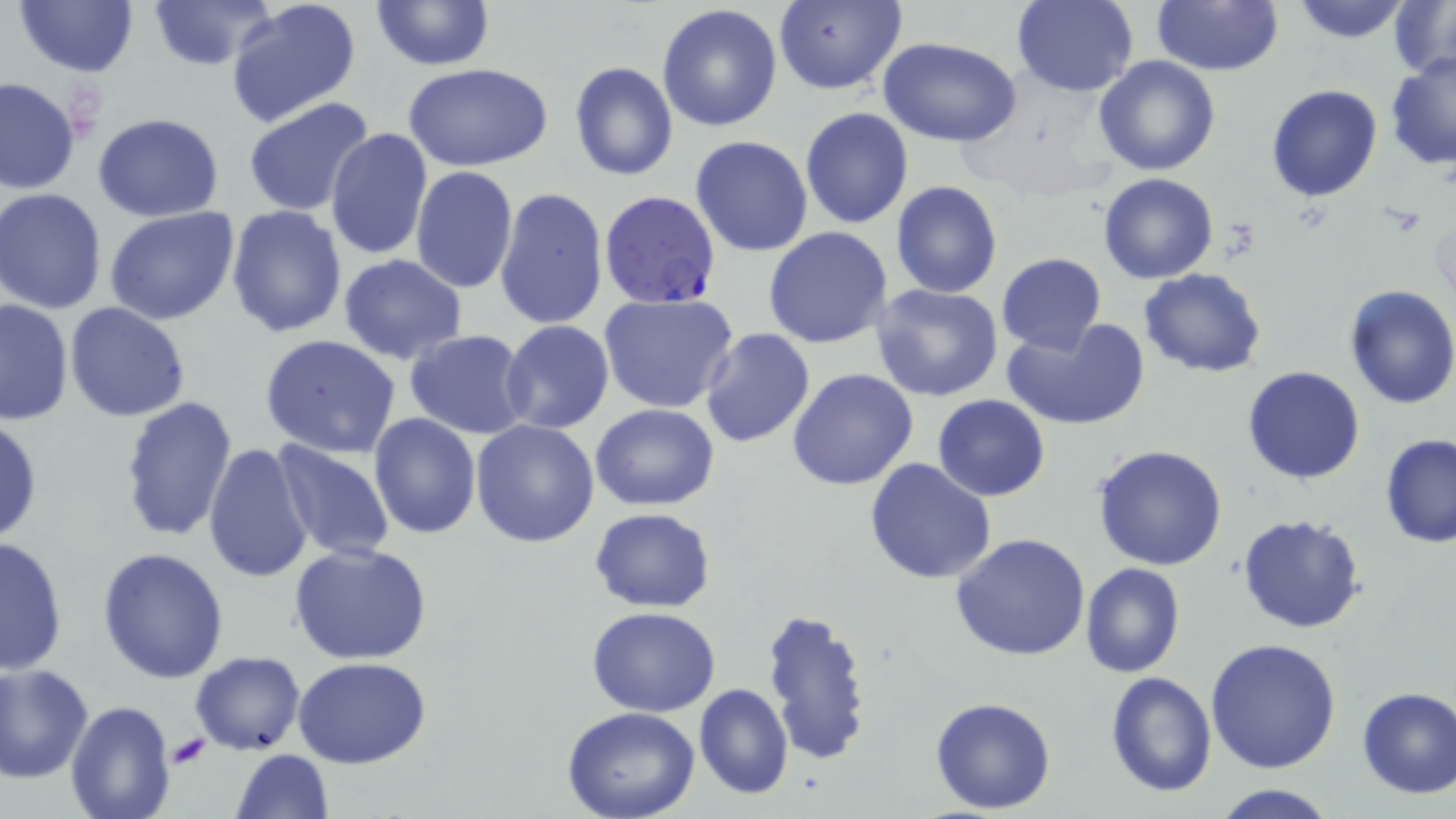

Approximate bounding boxes as (x1, y1, x2, y2) in pixels. Uninfected red blood cell locations: (13, 0, 140, 77), (148, 0, 278, 70), (225, 0, 363, 129), (369, 0, 494, 71), (773, 1, 907, 94), (1012, 1, 1139, 97), (1152, 1, 1284, 76), (1288, 1, 1415, 45), (1389, 1, 1456, 81), (658, 5, 784, 131), (878, 37, 1024, 147), (1385, 50, 1456, 170), (1093, 55, 1220, 176), (569, 61, 678, 182), (402, 62, 553, 171), (1, 77, 79, 195), (1266, 84, 1382, 202), (243, 95, 377, 215), (799, 106, 913, 230), (92, 114, 223, 220), (325, 127, 433, 259), (690, 136, 814, 257), (410, 166, 519, 295), (1098, 173, 1218, 284), (892, 182, 1002, 298), (496, 186, 609, 332), (1, 189, 111, 314), (226, 205, 346, 340), (103, 208, 241, 327), (764, 226, 894, 348), (996, 253, 1106, 355), (338, 255, 469, 366), (1139, 269, 1267, 377), (871, 283, 1003, 403), (1342, 284, 1456, 409), (598, 292, 740, 414), (0, 298, 74, 426), (65, 302, 192, 421), (1000, 317, 1149, 431), (500, 321, 615, 435), (700, 329, 815, 447), (404, 331, 531, 441), (259, 336, 403, 459), (1243, 365, 1366, 484), (788, 368, 918, 491), (934, 394, 1050, 502), (118, 395, 237, 542), (592, 404, 720, 511), (369, 412, 482, 540), (0, 416, 42, 546), (471, 420, 600, 547), (1380, 434, 1456, 549), (271, 441, 396, 562), (205, 442, 317, 585), (1092, 445, 1229, 572), (864, 456, 997, 584), (590, 507, 716, 612), (1237, 513, 1368, 635), (950, 531, 1092, 662), (0, 535, 69, 675), (290, 543, 434, 665), (99, 546, 230, 684), (1081, 563, 1186, 678), (1088, 563, 1195, 790), (587, 606, 720, 715), (760, 608, 875, 766), (1206, 637, 1342, 775), (191, 652, 305, 755), (294, 658, 433, 769), (1, 662, 94, 783), (1105, 671, 1217, 797), (693, 684, 793, 798), (1355, 684, 1456, 798), (929, 696, 1056, 813), (66, 700, 174, 819), (563, 709, 700, 819), (231, 749, 334, 818), (1207, 782, 1341, 819). Plasmodium falciparum-infected red blood cell locations: (602, 193, 726, 312). Platelet locations: (165, 733, 209, 770). Slide-level diagnosis: Plasmodium falciparum. Optical microscopy. Image is 1456×819 pixels. May-Grünwald-Giemsa-stained preparation. Thin blood film. Captured at 1000x magnification. Single field of view.